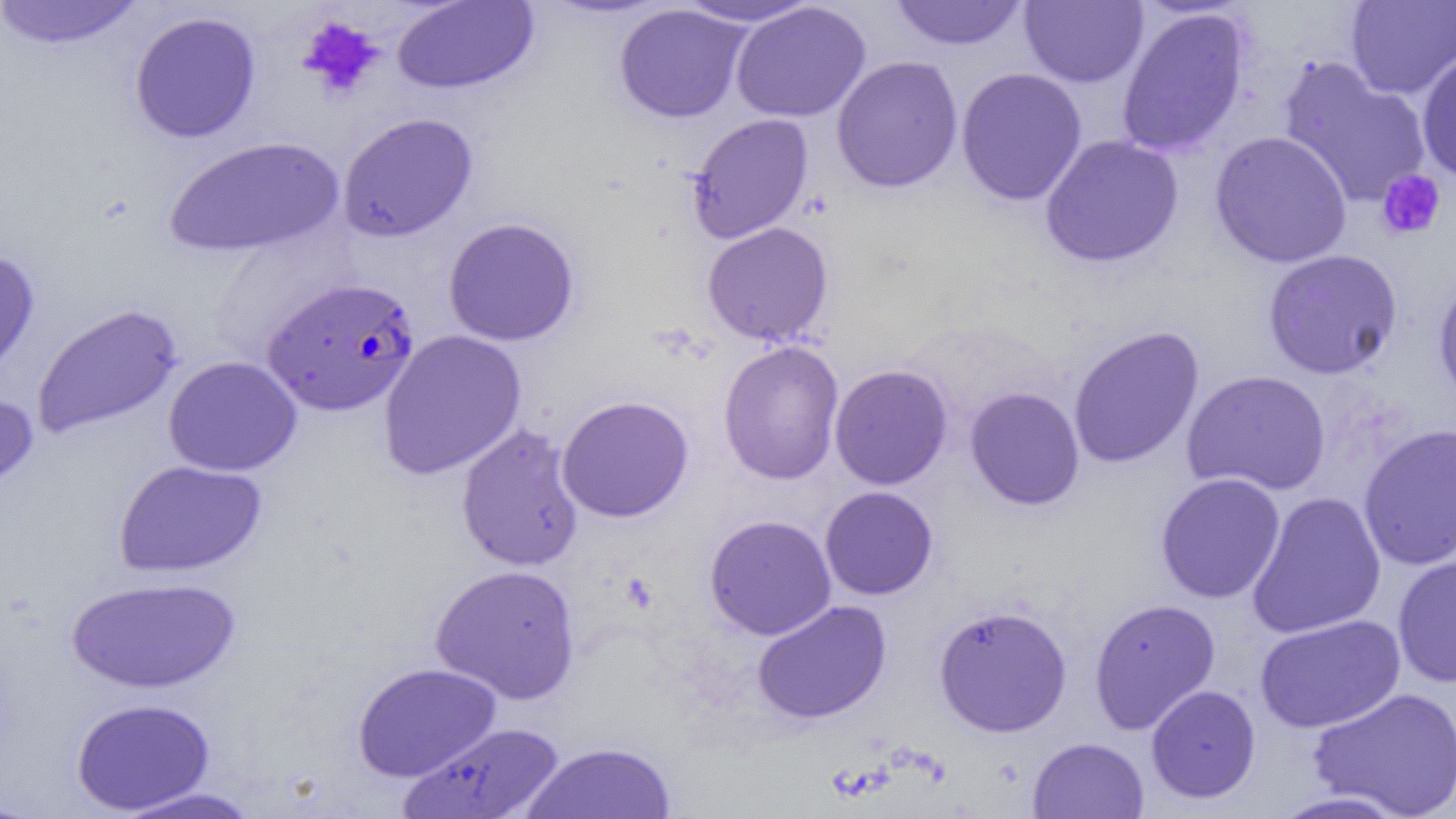
Approximate bounding boxes as (x1,y1)-(x2,y2) corner pairs in pixels. Platelet locations: (298,16)-(384,100), (1376,168)-(1446,241). Uninfected red blood cell locations: (0,0)-(146,49), (670,0)-(824,28), (391,1)-(538,94), (889,1)-(1030,50), (1020,1)-(1148,88), (1345,1)-(1456,99), (731,2)-(871,122), (614,4)-(751,123), (1116,6)-(1250,157), (129,11)-(261,143), (1415,48)-(1456,184), (831,55)-(964,193), (1277,56)-(1432,208), (956,67)-(1088,206), (337,112)-(478,242), (685,113)-(814,244), (1209,130)-(1352,268), (1040,134)-(1184,268), (163,136)-(344,258), (442,216)-(580,346), (701,221)-(834,346), (1262,248)-(1403,379), (0,249)-(41,388), (1433,273)-(1456,408), (30,303)-(183,439), (1068,325)-(1205,469), (377,329)-(527,480), (718,340)-(844,485), (163,356)-(302,477), (829,364)-(953,490), (1181,369)-(1331,496), (964,386)-(1085,510), (0,388)-(38,497), (557,395)-(694,523), (456,423)-(585,572), (1358,423)-(1456,570), (114,460)-(267,578), (1155,472)-(1286,604), (819,486)-(939,600), (1246,491)-(1387,639), (704,514)-(837,640), (1392,554)-(1456,687), (430,564)-(580,704), (65,575)-(240,694), (1088,598)-(1221,733), (752,600)-(892,724), (933,604)-(1072,737), (1254,614)-(1406,734), (352,662)-(502,782), (1146,684)-(1261,803), (1308,686)-(1456,817), (71,697)-(215,814), (398,723)-(565,818), (1027,737)-(1149,818), (519,740)-(677,819), (110,787)-(264,818), (1265,790)-(1412,818), (0,795)-(43,818). Plasmodium falciparum-infected red blood cell locations: (262,277)-(419,416). Slide-level diagnosis: Plasmodium falciparum. Thin blood smear. Captured at 1000x magnification. Light microscopy. One field of a larger specimen. Image is 1456×819 pixels.